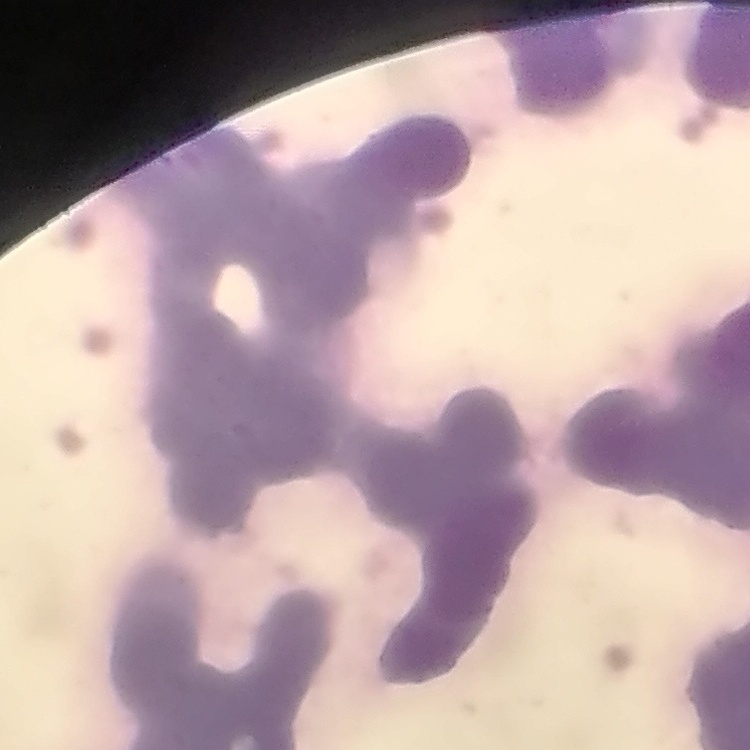

Summary:
  - Red blood cell morphology: rouleaux formation
  - Stain: Field's or Giemsa
  - Preparation: thin blood smear
  - Image type: square crop of a larger photomicrograph